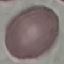 Malaria status: uninfected. Photographed with a smartphone camera at the microscope eyepiece. Automatically extracted cell patch, resized to 64 × 64 pixels. Thin smear of blood. Giemsa-stained preparation.